Locate malaria parasites and leukocytes.
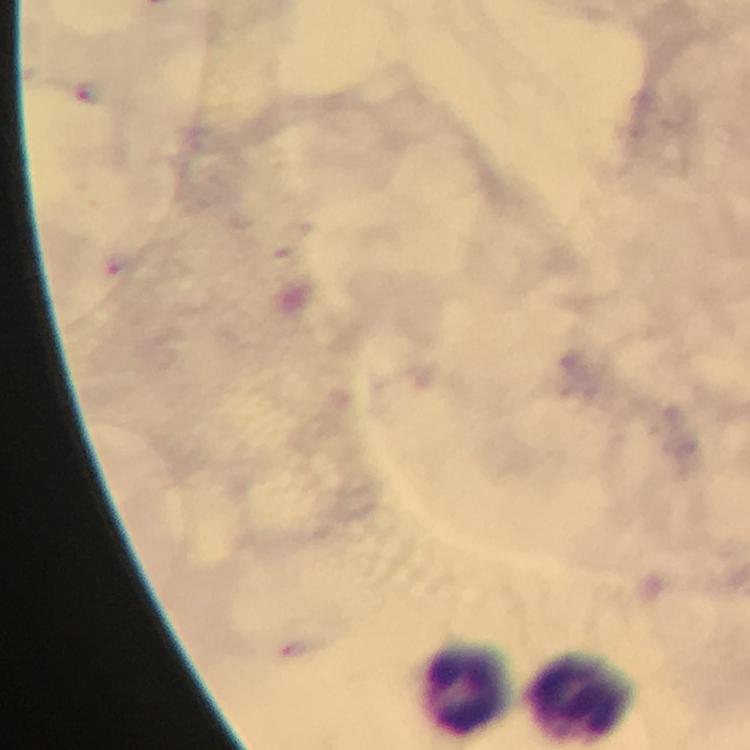

Approximate centers as (x, y) in pixels.
Malaria parasites: (91, 91), (116, 264).
Leukocytes: (465, 689), (580, 699).

context = from a diagnostic examination for malaria
preparation = thick blood film
magnification = 100x
stain = Giemsa
cropped from = one field of view
capture = smartphone photograph through a microscope
image size = 750×750 pixels
immersion oil = applied